Identify the blood parasite species.
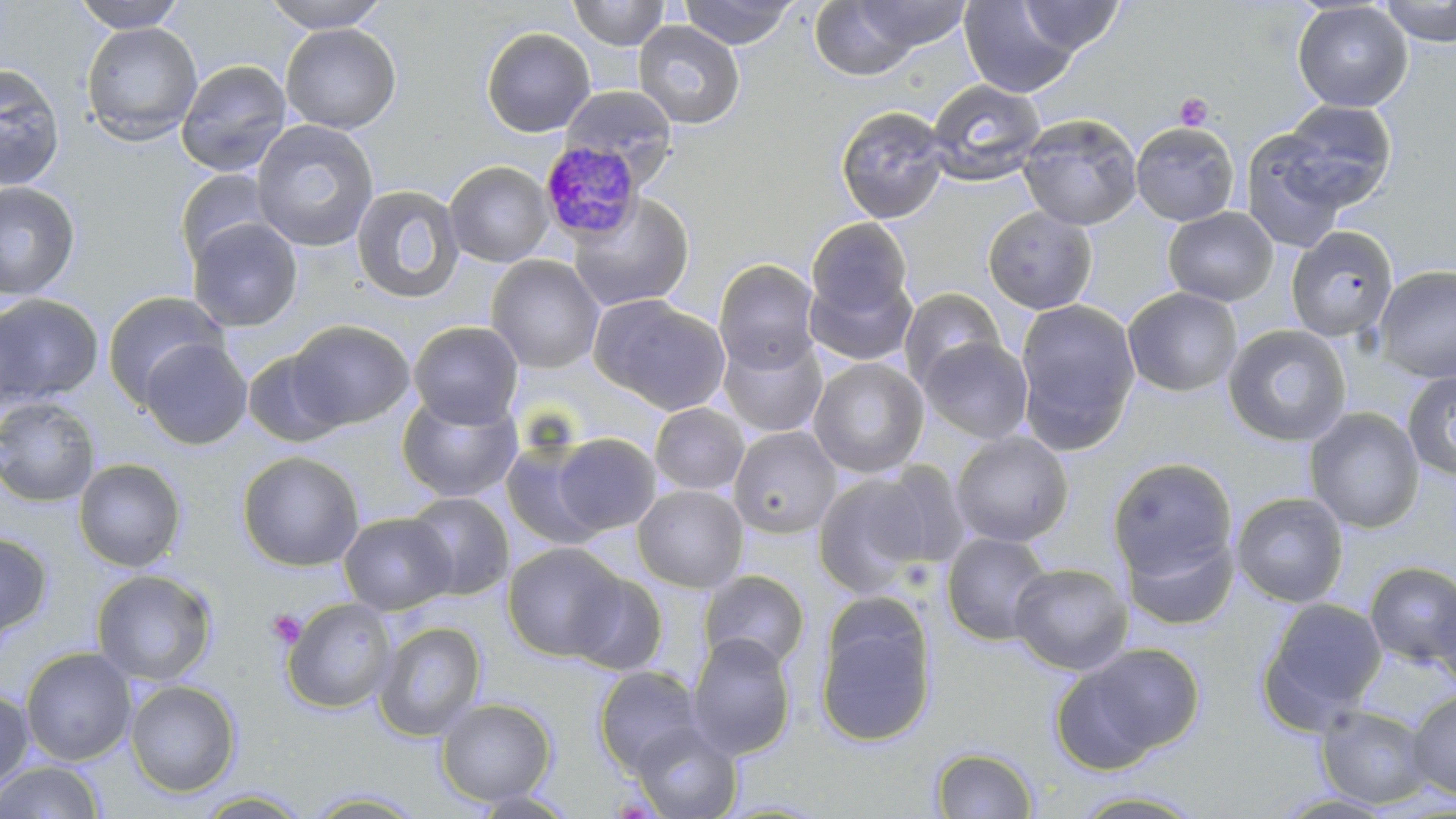

Plasmodium malariae.

Summary:
  - Coordinate format: approximate bounding boxes as [x1, y1, x2, y2] in pixels
  - Uninfected red blood cell locations: [71, 0, 188, 32], [260, 0, 392, 32], [567, 0, 670, 50], [678, 0, 799, 49], [1379, 0, 1456, 46], [808, 1, 927, 81], [846, 1, 972, 53], [960, 1, 1080, 98], [1018, 1, 1125, 55], [1292, 1, 1413, 112], [632, 20, 745, 130], [80, 21, 203, 145], [280, 23, 401, 134], [480, 26, 595, 138], [175, 59, 292, 177], [0, 63, 65, 190], [926, 78, 1046, 186], [558, 85, 679, 186], [1279, 100, 1397, 209], [835, 105, 951, 224], [1017, 113, 1143, 230], [251, 119, 380, 252], [1130, 122, 1240, 226], [1239, 130, 1352, 252], [444, 161, 553, 268], [174, 169, 280, 269], [0, 180, 81, 301], [351, 184, 464, 304], [565, 192, 696, 313], [982, 205, 1098, 315], [1163, 207, 1279, 306], [187, 217, 303, 332], [806, 217, 914, 319], [1286, 226, 1398, 341], [486, 254, 605, 374], [713, 258, 822, 375], [1374, 264, 1456, 383], [805, 270, 916, 367], [1122, 287, 1243, 397], [898, 288, 1005, 389], [102, 290, 230, 407], [0, 294, 104, 409], [590, 295, 731, 415], [1014, 298, 1141, 449], [1, 306, 39, 416], [287, 319, 414, 430], [408, 321, 524, 429], [1222, 323, 1353, 447], [718, 334, 828, 438], [918, 336, 1034, 445], [139, 338, 253, 450], [242, 347, 348, 447], [807, 357, 930, 479], [1402, 371, 1456, 483], [396, 392, 522, 503], [0, 396, 101, 507], [650, 403, 750, 496], [1304, 407, 1424, 534], [728, 426, 842, 539], [950, 431, 1074, 547], [551, 432, 661, 535], [500, 439, 607, 551], [237, 451, 364, 571], [1106, 457, 1238, 584], [73, 458, 187, 572], [868, 461, 973, 570], [812, 469, 943, 598], [632, 484, 749, 593], [404, 491, 514, 600], [1231, 492, 1349, 608], [338, 512, 456, 615], [1121, 527, 1238, 631], [0, 530, 52, 641], [940, 531, 1054, 646], [501, 542, 629, 662], [1364, 560, 1456, 667], [1009, 562, 1133, 675], [91, 568, 218, 687], [567, 569, 670, 676], [698, 570, 810, 671], [1432, 583, 1456, 692], [281, 596, 397, 714], [1258, 597, 1387, 731], [814, 599, 937, 749], [373, 621, 487, 741], [687, 632, 796, 760], [1055, 642, 1204, 769], [21, 647, 137, 767], [593, 665, 705, 775], [125, 679, 241, 797], [0, 687, 35, 792], [1405, 690, 1456, 800], [435, 697, 557, 806], [1315, 704, 1434, 809], [629, 721, 742, 819], [931, 747, 1038, 818], [0, 760, 106, 818], [191, 789, 312, 818], [301, 789, 426, 817], [464, 789, 582, 818], [1065, 789, 1208, 818]
  - Plasmodium malariae-infected red blood cell locations: [544, 140, 650, 254]
  - Platelet locations: [1174, 92, 1214, 131], [267, 609, 308, 648]
  - Stain: May-Grünwald-Giemsa
  - Preparation: thin blood smear
  - Modality: light microscopy
  - Magnification: 1000x
  - Field of view: one of a larger specimen
  - Image size: 1456×819 pixels